Comment on the morphology of the red blood cells.
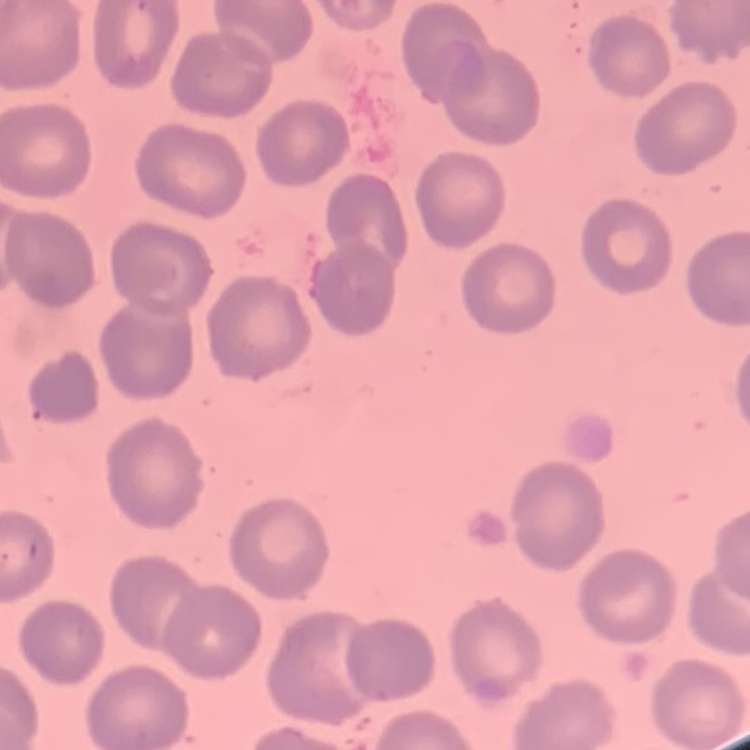

They show no rouleaux formation.

Summary:
  - Preparation: thin blood film
  - Stain: Field's or Giemsa
  - Image type: square crop of a larger photomicrograph